Identify the cell.
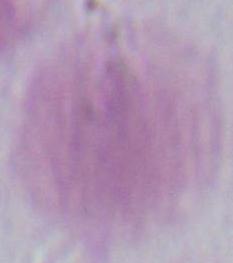
An erythrocyte.

Micrograph. 1000x magnification.